Comment on the morphology of the red blood cells.
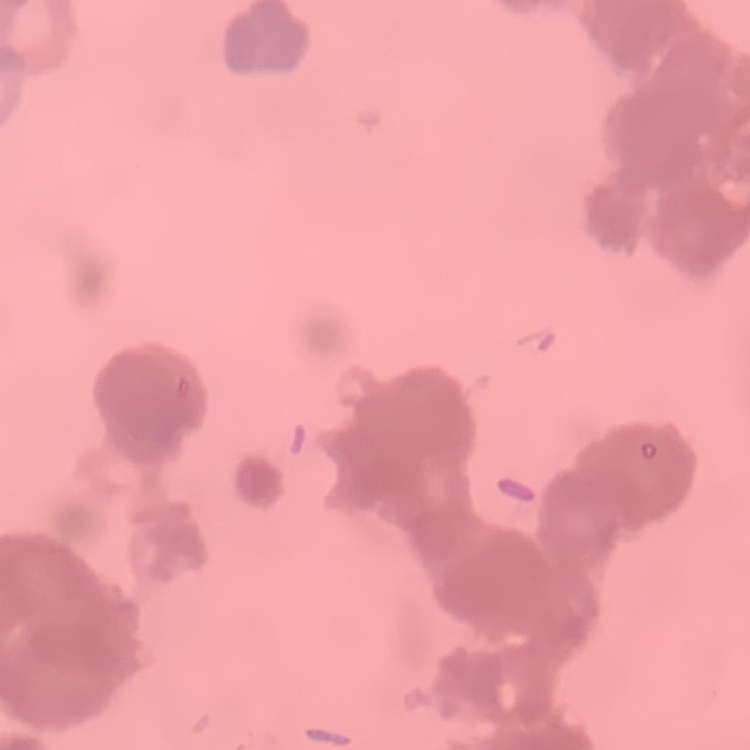
They show rouleaux formation.

Summary:
  - Preparation: thin blood smear
  - Image type: one tile cut from a larger photomicrograph
  - Stain: Field's or Giemsa